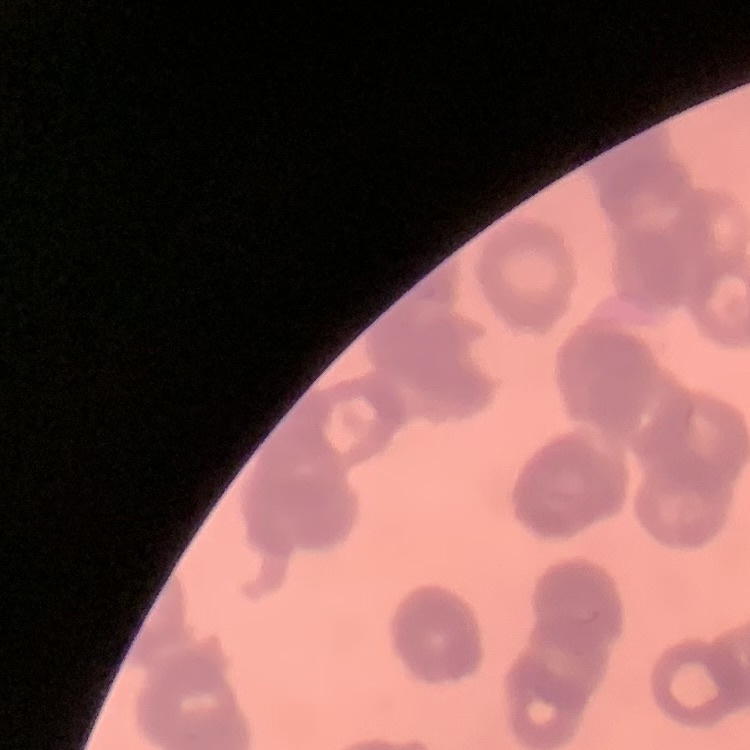
{
  "erythrocyte_morphology": "rouleaux formation",
  "image_type": "one tile cut from a larger photomicrograph",
  "preparation": "thin blood smear",
  "stain": "Field's or Giemsa"
}